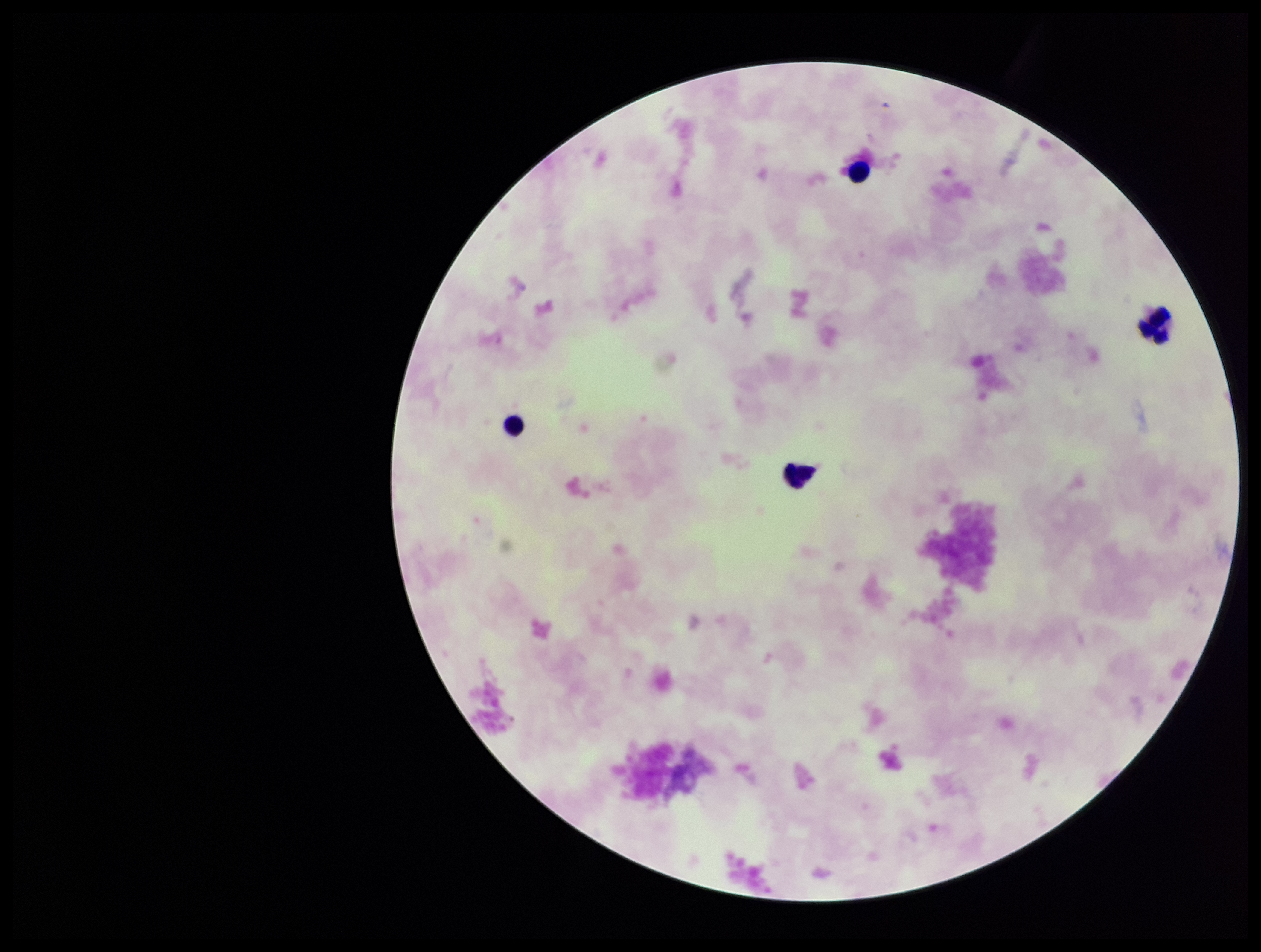
Stained with Giemsa. Single field of view. Patient malaria status: negative. Preparation: thick smear. Plasmodium parasites: none seen. Leukocyte count: 4. Parasite count: 0. Smartphone photograph taken through the eyepiece of a microscope. Image is 1261×952 pixels.